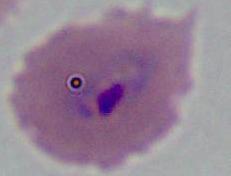
Summary:
  - Identification: Plasmodium
  - Modality: micrograph
  - Magnification: 400x or 1000x